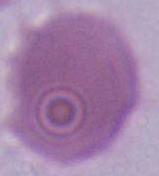
Photomicrograph. An erythrocyte is shown. 1000x magnification.